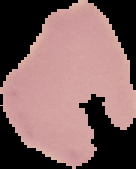 Image is 136×169 pixels. From a thin blood film. Malaria status: uninfected. Cell region segmented out of the field of view; the surrounding area is masked to black.